Describe the morphology of the red blood cells.
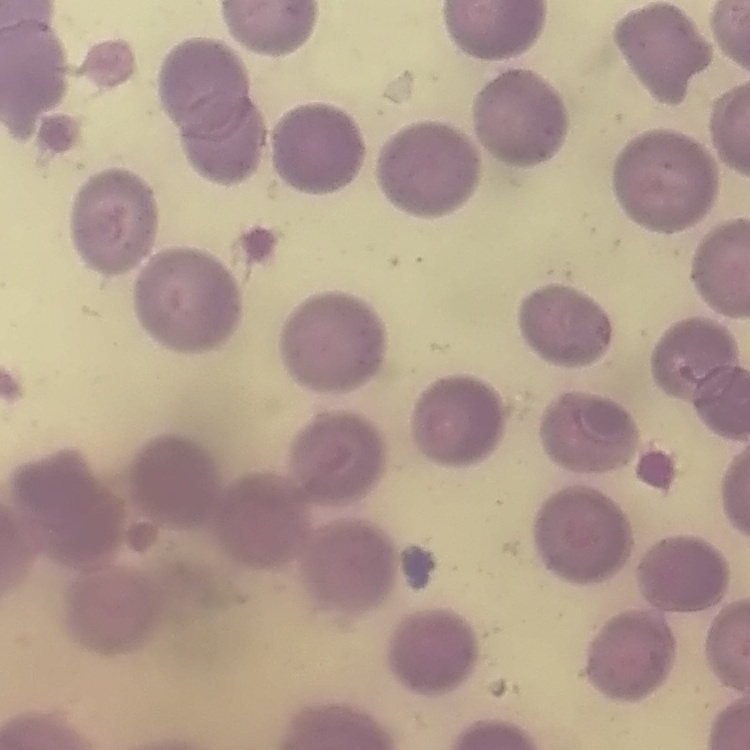

No rouleaux formation.

Thin blood film. Square crop of a larger photomicrograph. Stained with either Field's or Giemsa.